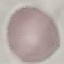

malaria_status: uninfected
preparation: thin blood film
capture: smartphone camera at the microscope eyepiece
image_type: automatically extracted cell patch, resized to 64 × 64 pixels
stain: Giemsa